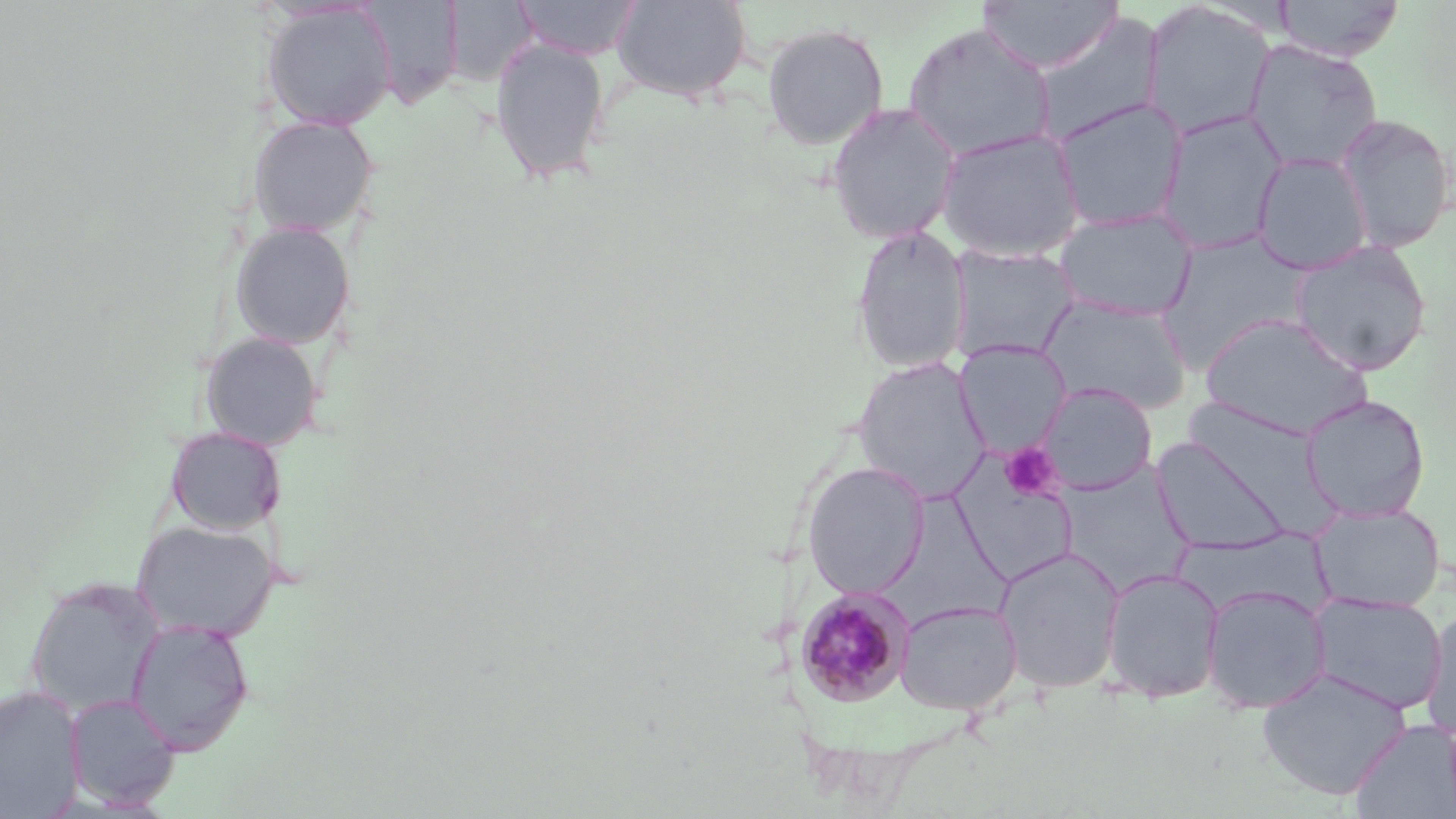

slide-level diagnosis = Plasmodium malariae
stain = May-Grünwald-Giemsa
uninfected red blood cell locations = approximate bounding boxes as named x1/y1/x2/y2 corners in pixels: (x1=357, y1=0, x2=465, y2=110), (x1=611, y1=0, x2=752, y2=102), (x1=977, y1=0, x2=1122, y2=75), (x1=1273, y1=0, x2=1405, y2=61), (x1=442, y1=1, x2=536, y2=89), (x1=513, y1=1, x2=642, y2=60), (x1=1140, y1=1, x2=1276, y2=141), (x1=259, y1=3, x2=397, y2=131), (x1=1034, y1=13, x2=1166, y2=146), (x1=902, y1=22, x2=1056, y2=162), (x1=761, y1=23, x2=889, y2=150), (x1=488, y1=34, x2=611, y2=186), (x1=1243, y1=39, x2=1383, y2=172), (x1=1053, y1=98, x2=1188, y2=233), (x1=825, y1=101, x2=962, y2=245), (x1=1157, y1=110, x2=1287, y2=257), (x1=1333, y1=112, x2=1455, y2=254), (x1=246, y1=114, x2=380, y2=238), (x1=936, y1=128, x2=1085, y2=263), (x1=1251, y1=152, x2=1372, y2=275), (x1=1053, y1=209, x2=1197, y2=321), (x1=229, y1=221, x2=357, y2=350), (x1=850, y1=224, x2=972, y2=376), (x1=1290, y1=239, x2=1432, y2=376), (x1=945, y1=245, x2=1079, y2=364), (x1=1038, y1=294, x2=1192, y2=416), (x1=1198, y1=312, x2=1372, y2=438), (x1=198, y1=332, x2=325, y2=451), (x1=955, y1=342, x2=1070, y2=456), (x1=852, y1=356, x2=990, y2=503), (x1=1037, y1=381, x2=1157, y2=495), (x1=1300, y1=393, x2=1430, y2=523), (x1=164, y1=425, x2=286, y2=536), (x1=1150, y1=435, x2=1293, y2=555), (x1=957, y1=446, x2=1075, y2=584), (x1=802, y1=461, x2=929, y2=599), (x1=1058, y1=463, x2=1194, y2=593), (x1=885, y1=486, x2=1020, y2=632), (x1=1311, y1=503, x2=1446, y2=613), (x1=131, y1=519, x2=279, y2=641), (x1=1174, y1=529, x2=1333, y2=619), (x1=994, y1=546, x2=1125, y2=693), (x1=1101, y1=567, x2=1225, y2=703), (x1=23, y1=576, x2=164, y2=717), (x1=1201, y1=584, x2=1331, y2=714), (x1=1309, y1=592, x2=1447, y2=713), (x1=895, y1=600, x2=1022, y2=714), (x1=1420, y1=606, x2=1456, y2=742), (x1=125, y1=618, x2=255, y2=755), (x1=1256, y1=667, x2=1412, y2=800), (x1=0, y1=685, x2=85, y2=818), (x1=64, y1=693, x2=181, y2=810), (x1=1349, y1=719, x2=1456, y2=817)
platelet locations = approximate bounding boxes as named x1/y1/x2/y2 corners in pixels: (x1=1000, y1=443, x2=1062, y2=501)
modality = optical microscopy
magnification = 1000x
Plasmodium malariae-infected red blood cell locations = approximate bounding boxes as named x1/y1/x2/y2 corners in pixels: (x1=795, y1=586, x2=915, y2=706)
field of view = single
preparation = thin blood smear
image size = 1456×819 pixels